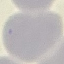
malaria status = uninfected
image type = automatically extracted cell patch, resized to 64 × 64 pixels
capture = smartphone through the microscope eyepiece
stain = Giemsa
preparation = thin blood film